Describe the morphology of the red blood cells.
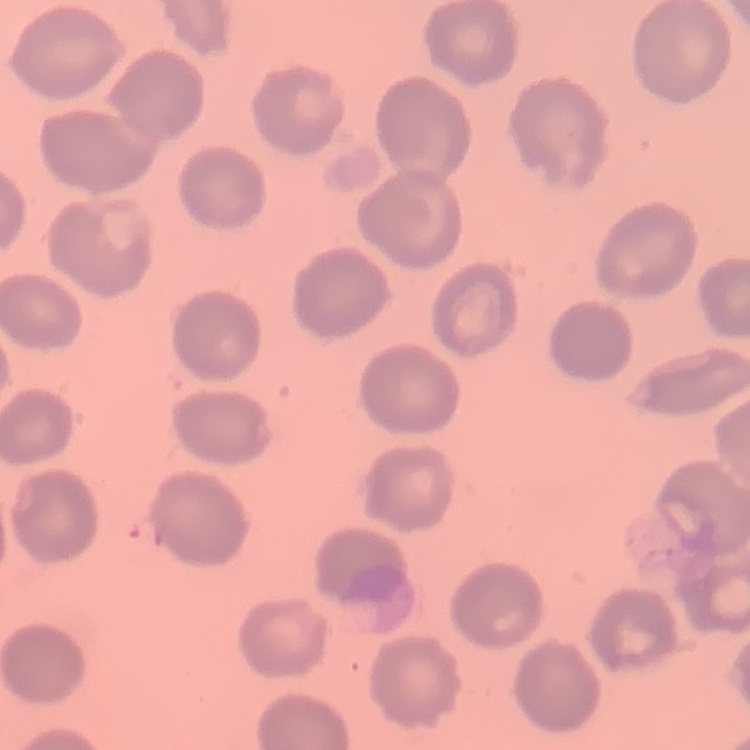

They show no rouleaux formation.

Thin blood smear. Square crop of a larger photomicrograph. Stained with either Field's or Giemsa.